Comment on the morphology of the erythrocytes.
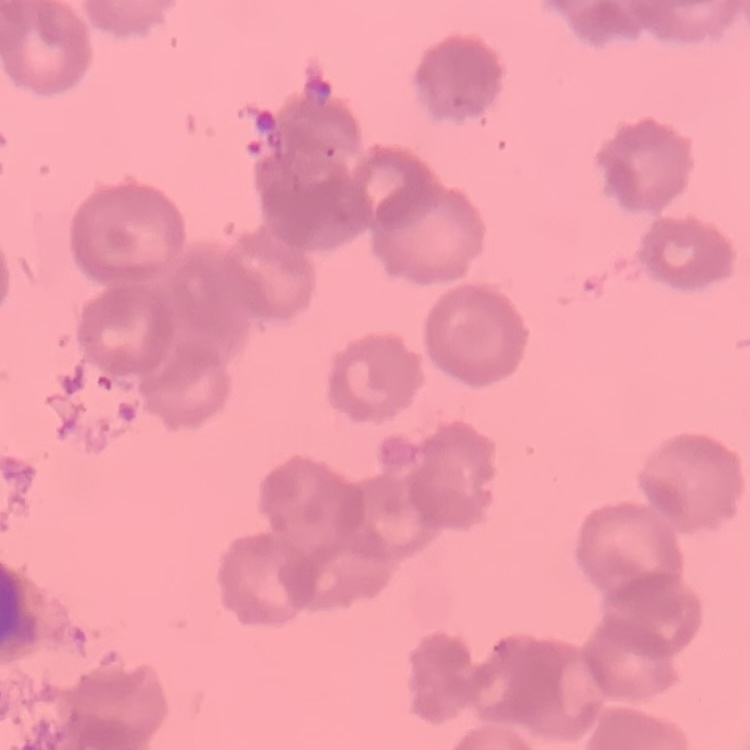

Rouleaux formation.

Field's or Giemsa stain. Thin blood film. Square crop of a larger photomicrograph.